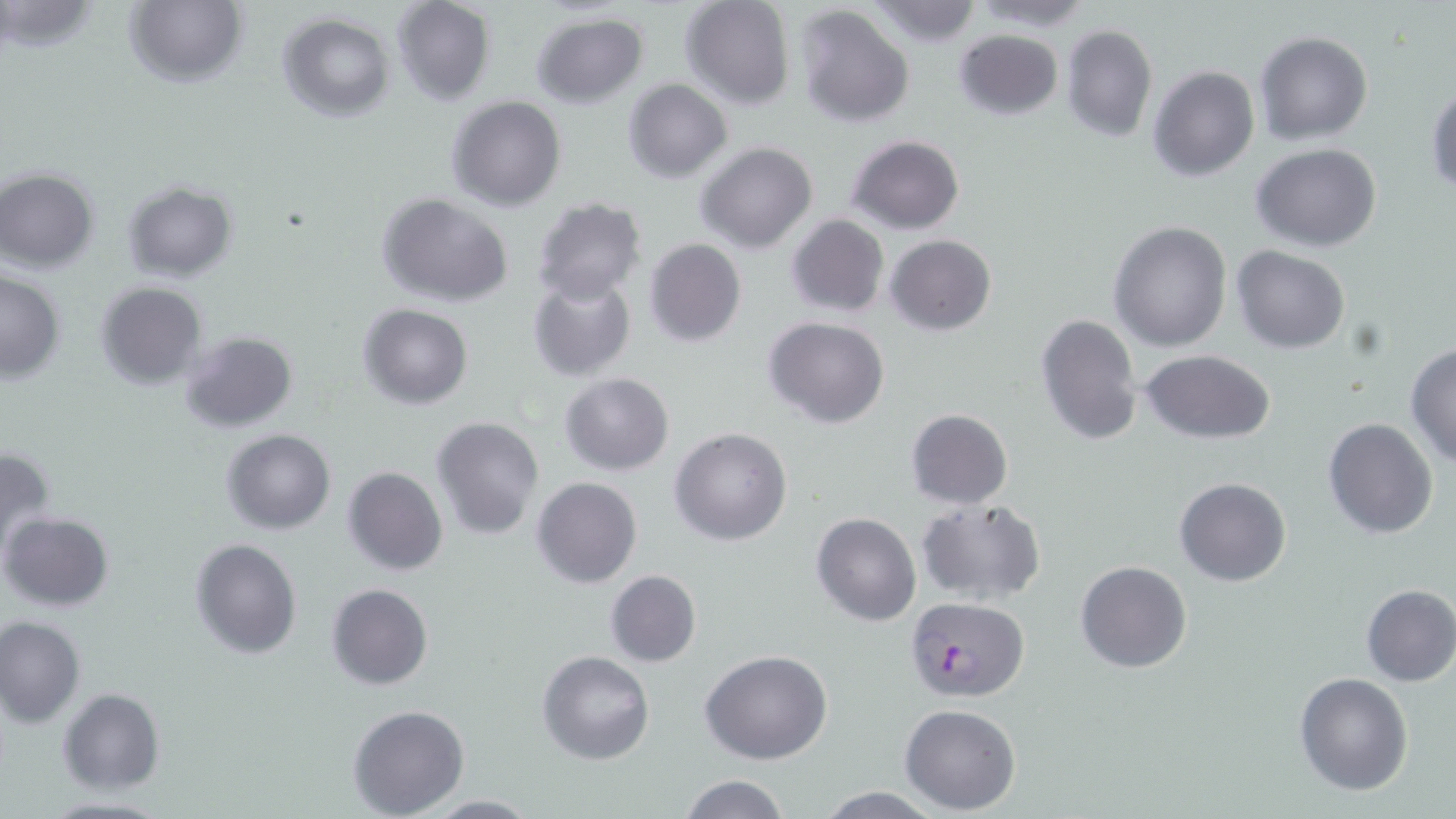

Approximate bounding boxes as [x1, y1, x2, y2] in pixels. Plasmodium falciparum-infected red blood cell locations: [907, 598, 1030, 701]. Uninfected red blood cell locations: [390, 0, 497, 105], [679, 0, 795, 109], [970, 0, 1098, 31], [1, 1, 100, 53], [124, 1, 246, 88], [867, 1, 983, 48], [795, 5, 916, 128], [531, 12, 650, 108], [278, 14, 395, 122], [1060, 23, 1157, 142], [953, 29, 1063, 121], [1254, 31, 1373, 146], [1149, 65, 1259, 182], [623, 78, 732, 183], [1426, 86, 1456, 196], [446, 96, 565, 210], [847, 135, 963, 234], [696, 141, 818, 253], [1252, 142, 1382, 252], [0, 170, 99, 272], [122, 180, 239, 282], [376, 193, 515, 309], [532, 197, 647, 304], [786, 215, 889, 318], [1109, 222, 1231, 352], [886, 235, 996, 335], [645, 238, 746, 348], [1230, 246, 1349, 353], [0, 269, 64, 383], [527, 273, 636, 383], [93, 281, 208, 390], [358, 303, 472, 410], [1034, 312, 1142, 448], [764, 317, 889, 428], [178, 330, 300, 435], [1405, 342, 1456, 467], [1141, 348, 1276, 444], [559, 372, 674, 475], [905, 409, 1013, 509], [431, 417, 543, 538], [1321, 417, 1438, 539], [670, 426, 793, 546], [221, 429, 334, 534], [0, 445, 57, 563], [342, 467, 449, 577], [533, 477, 641, 589], [1174, 477, 1291, 587], [915, 499, 1046, 603], [1, 512, 114, 611], [811, 512, 922, 626], [190, 538, 302, 659], [1075, 559, 1193, 673], [605, 570, 701, 667], [326, 583, 433, 690], [1359, 584, 1456, 686], [1, 615, 86, 726], [701, 648, 833, 765], [537, 650, 654, 765], [1294, 672, 1414, 794], [58, 689, 166, 795], [349, 704, 469, 817], [899, 704, 1022, 814], [677, 775, 795, 819], [812, 785, 949, 819], [422, 794, 539, 817], [40, 795, 172, 817]. Slide-level diagnosis: Plasmodium falciparum. May-Grünwald-Giemsa-stained preparation. Light microscopy. Thin blood film. 1000x magnification. Image is 1456×819 pixels. Single field of view.